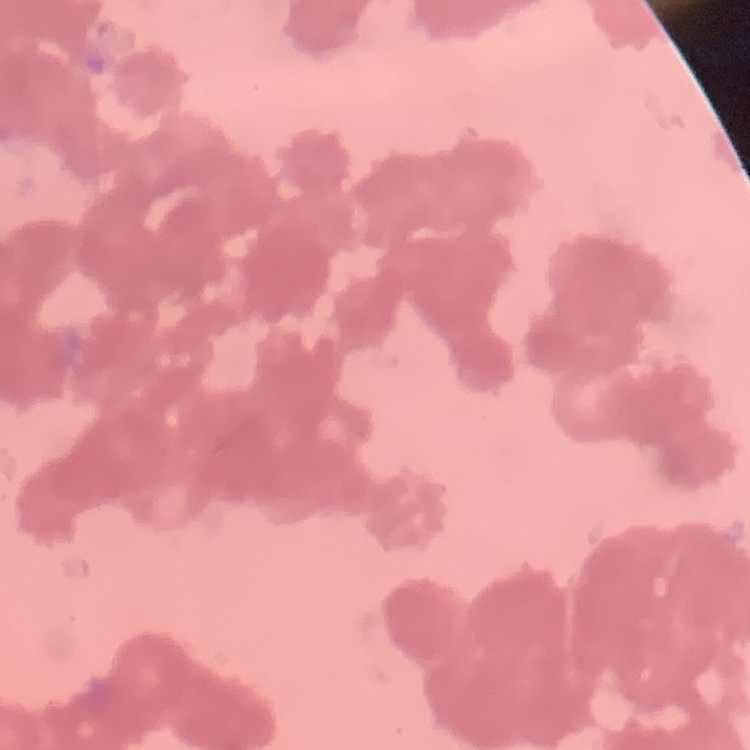
Summary:
  - Erythrocyte morphology: rouleaux formation
  - Preparation: thin blood film
  - Image type: square crop of a larger photomicrograph
  - Stain: Field's or Giemsa